Classify this cell by malaria status.
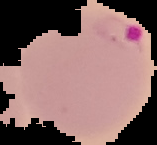

It is parasitized.

{
  "image_size": "157×145 pixels",
  "image_type": "segmented cell region on a black background",
  "preparation": "thin blood smear"
}